Evaluate for malaria.
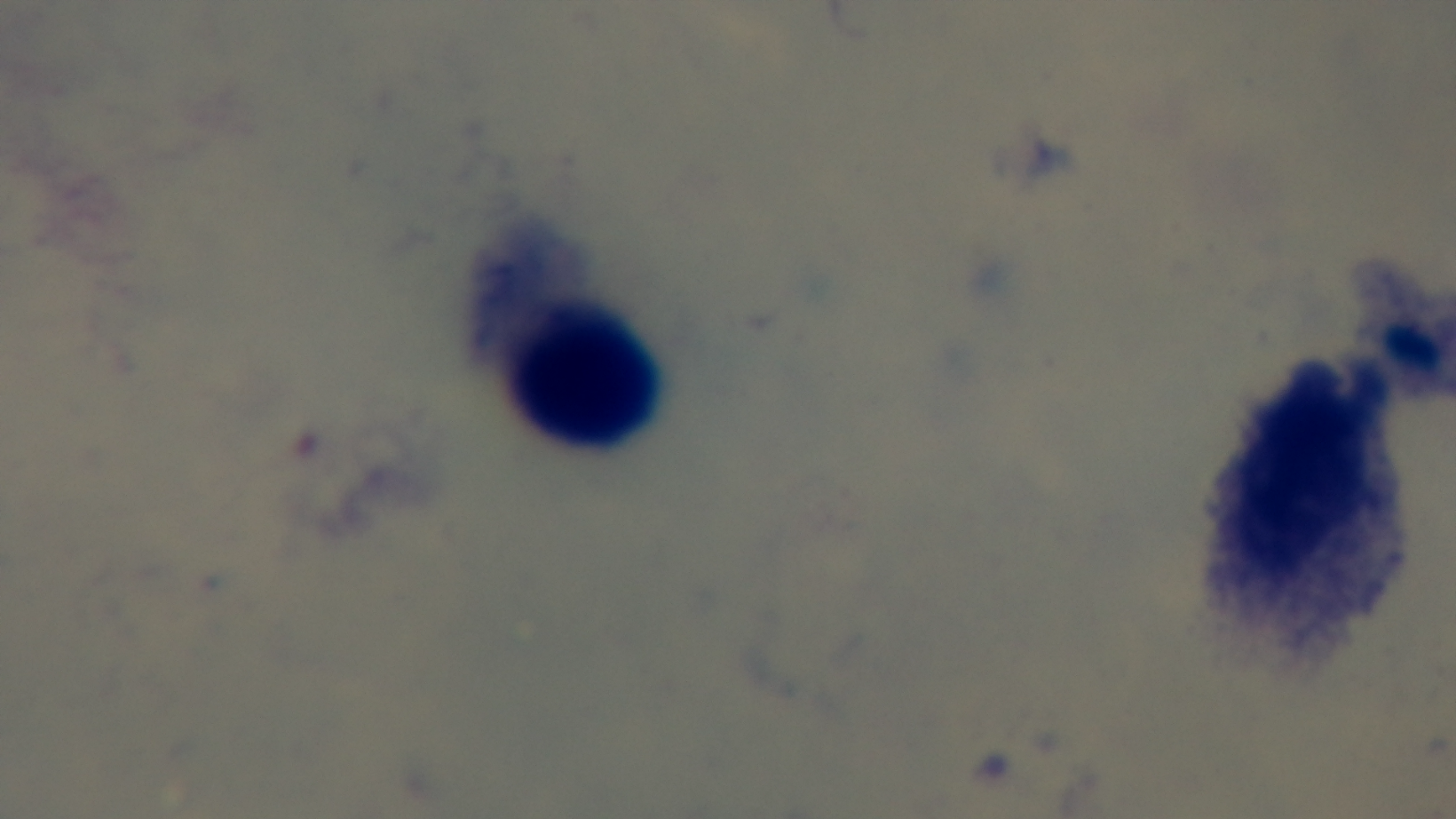

It is uninfected.

modality: light microscopy
stain: Giemsa
preparation: thick
capture: mounted 4K digital camera
field_of_view: one from the slide
objective: 100x oil immersion